Look for parasitized red blood cells.
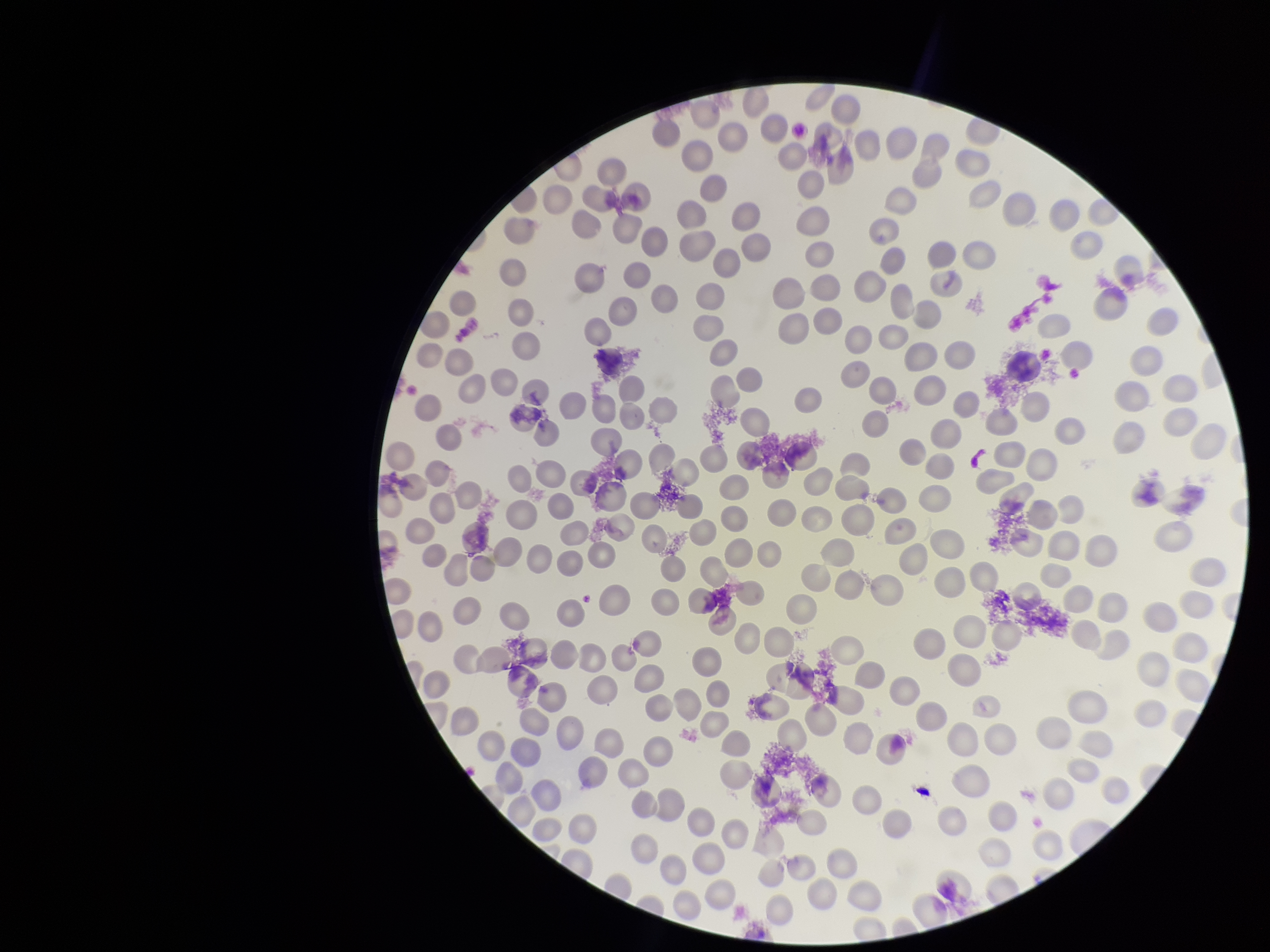
None seen.

Summary:
  - Stain: Giemsa
  - Patient malaria status: negative
  - Image size: 1270×952 pixels
  - Capture: smartphone photograph through the microscope eyepiece
  - Preparation: thin blood smear
  - Parasitized red blood cell count: 0
  - Field of view: single
  - Red blood cell count: 235